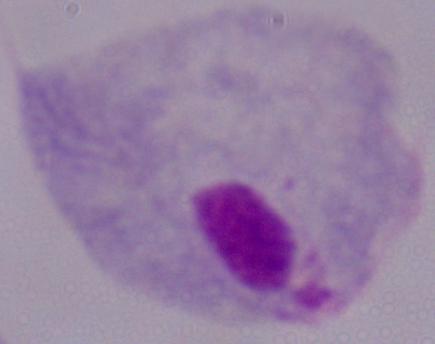
{
  "identification": "trichomonad",
  "modality": "micrograph",
  "magnification": "1000x"
}